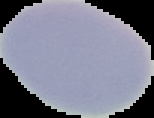

Summary:
  - Preparation: thin blood film
  - Malaria status: uninfected
  - Image size: 154×118 pixels
  - Image type: cell region segmented out of the field of view; surrounding area masked to black